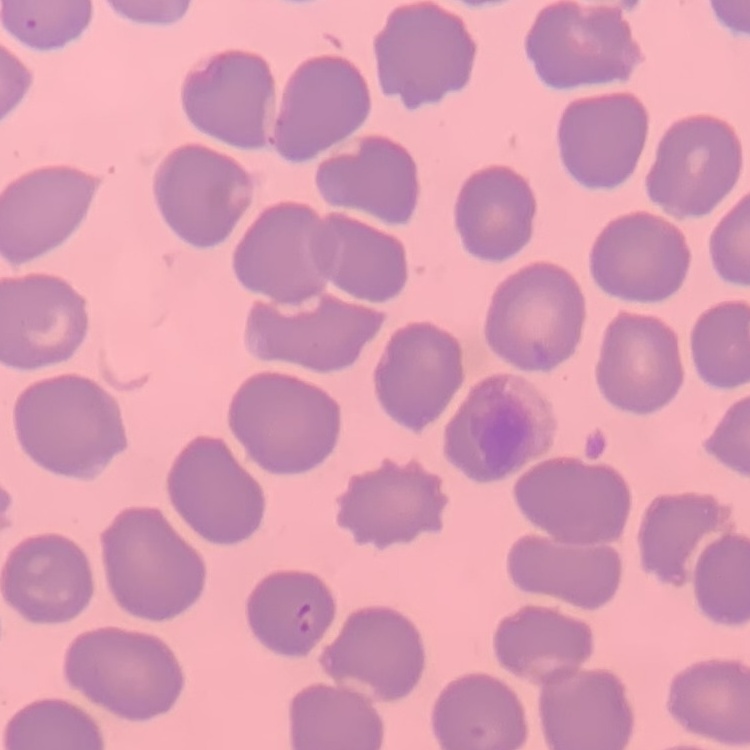
Summary:
  - Red blood cell morphology: no rouleaux formation
  - Preparation: thin peripheral smear
  - Stain: Field's or Giemsa
  - Image type: square crop of a larger photomicrograph